Give the extent of the Plasmodium ovale parasites you find, grouped by life-cycle stage — ring form, trophozoite, schizont, or gametocyte.
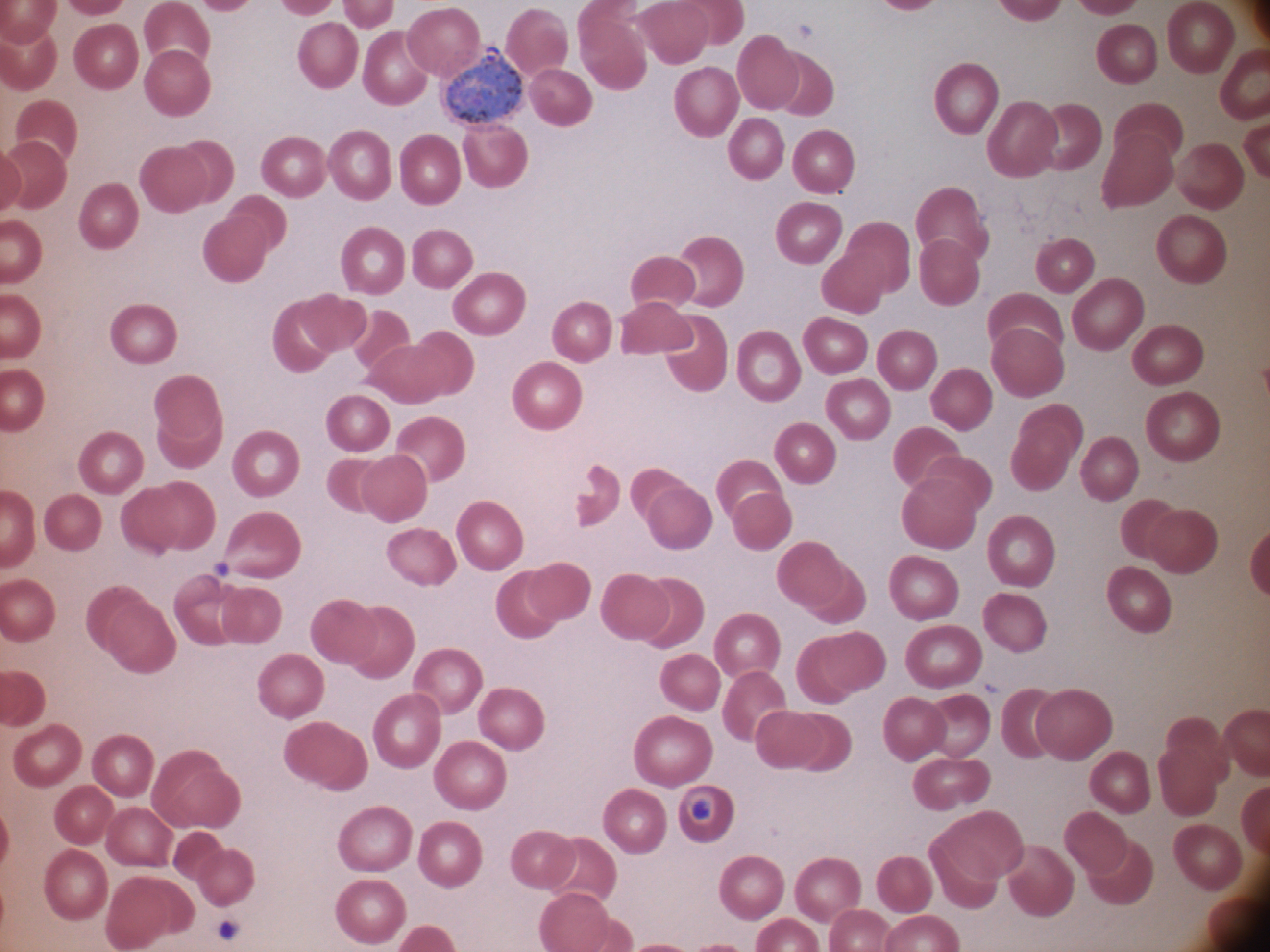
Approximate bounding boxes as named x1/y1/x2/y2 corners in pixels, from the source annotation, which is not necessarily exhaustive.
Gametocytes: (x1=445, y1=44, x2=524, y2=128).

Summary:
  - Microscope: Leica DM2000 with built-in camera
  - Image size: 1270×952 pixels
  - Preparation: thin blood film
  - Magnification: 100x
  - Stain: Giemsa
  - Species: Plasmodium ovale
  - Field of view: single